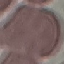
Malaria status: uninfected. Acquired by smartphone through the microscope eyepiece. Automatically extracted cell patch, resized to 64 × 64 pixels. Giemsa stain. Thin blood smear.